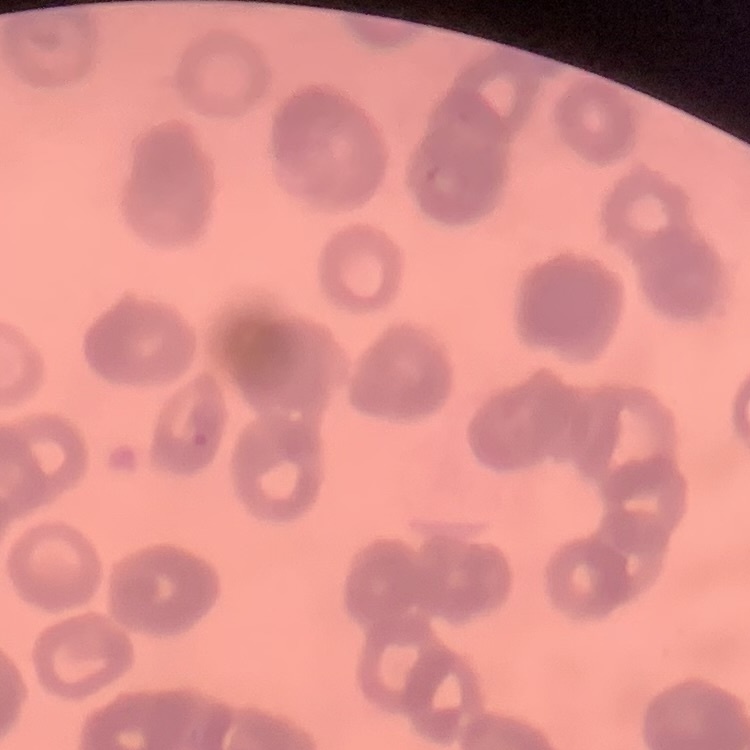

Summary:
  - Erythrocyte morphology: rouleaux formation
  - Preparation: thin blood film
  - Image type: one tile cut from a larger photomicrograph
  - Stain: Field's or Giemsa